Classify this cell by malaria status.
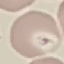

Parasitized.

stain: Giemsa
preparation: thin smear
capture: smartphone camera at the microscope eyepiece
image_type: cell patch, automatically extracted from a larger field of view and resized to 64 × 64 pixels